Locate every blood parasite and identify its species.
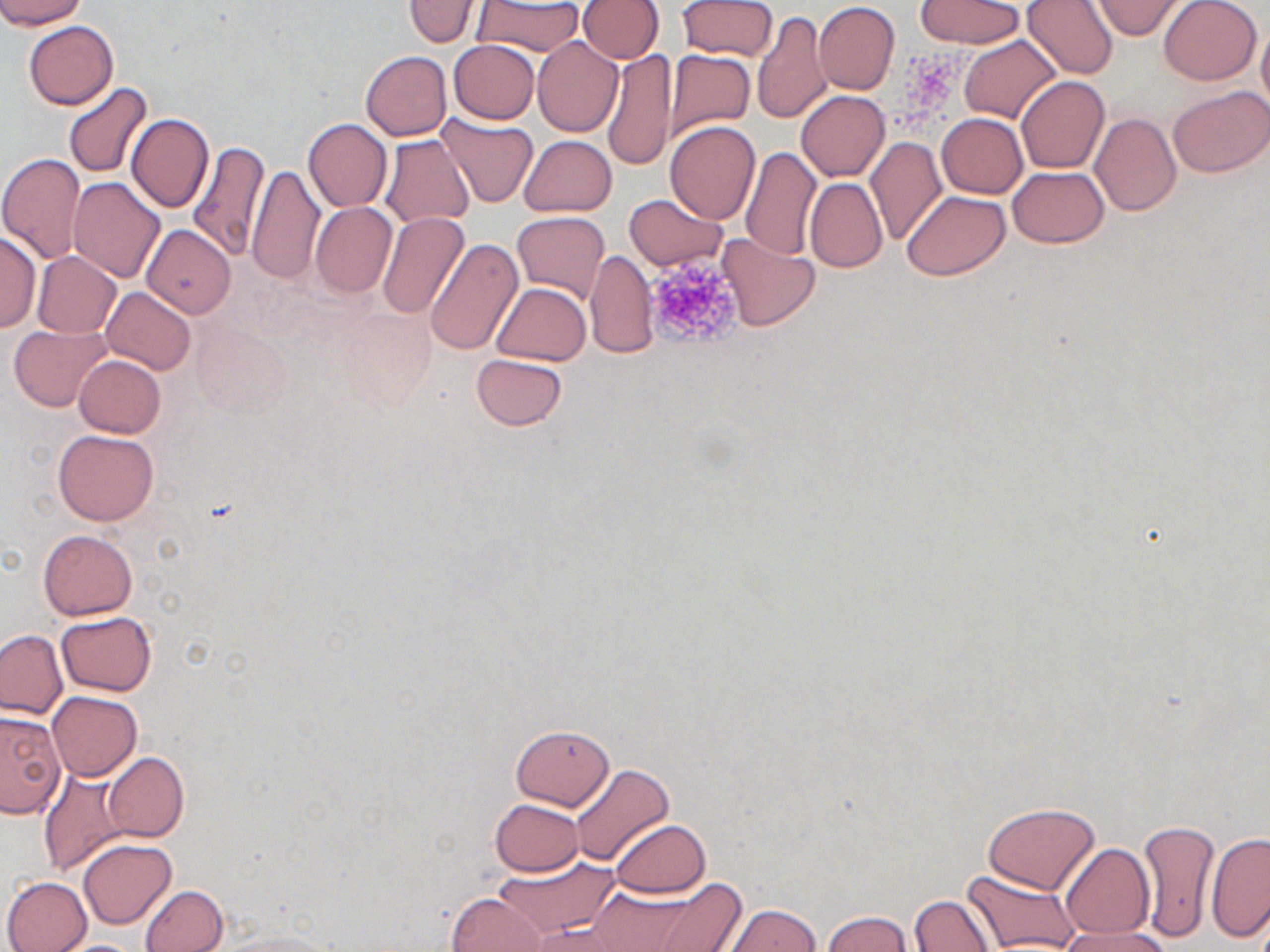
No blood parasites observed.

Summary:
  - Coordinate format: approximate bounding boxes as [x1, y1, x2, y2] in pixels
  - Platelet locations: [644, 255, 745, 350]
  - Uninfected red blood cell locations: [0, 0, 86, 28], [577, 0, 664, 64], [1022, 0, 1119, 79], [1159, 0, 1262, 86], [404, 1, 481, 47], [474, 1, 586, 57], [679, 1, 778, 60], [916, 1, 1026, 48], [1091, 1, 1186, 39], [813, 2, 900, 94], [752, 11, 832, 124], [1257, 19, 1270, 123], [23, 21, 119, 109], [959, 36, 1061, 124], [532, 37, 624, 136], [449, 40, 539, 123], [602, 49, 677, 171], [664, 50, 755, 139], [361, 51, 452, 140], [1016, 77, 1108, 173], [644, 78, 736, 210], [63, 82, 152, 177], [1169, 86, 1270, 178], [797, 90, 889, 181], [436, 112, 538, 208], [936, 113, 1027, 198], [1091, 113, 1180, 215], [126, 114, 214, 213], [303, 118, 391, 211], [664, 120, 760, 223], [379, 134, 474, 229], [519, 135, 617, 217], [864, 136, 946, 247], [186, 141, 271, 261], [741, 147, 821, 261], [0, 154, 87, 265], [247, 163, 324, 287], [1007, 166, 1109, 247], [67, 176, 165, 281], [805, 178, 887, 272], [901, 190, 1010, 279], [624, 194, 727, 271], [311, 203, 397, 298], [512, 211, 610, 303], [376, 213, 469, 319], [140, 225, 236, 318], [0, 230, 40, 333], [716, 232, 820, 331], [424, 238, 525, 355], [585, 250, 656, 358], [31, 251, 122, 338], [491, 282, 591, 365], [101, 285, 195, 375], [193, 320, 292, 416], [9, 324, 111, 412], [471, 353, 567, 431], [74, 354, 165, 438], [53, 429, 158, 525], [40, 529, 138, 619], [55, 612, 156, 695], [0, 629, 67, 719], [47, 690, 142, 780], [0, 709, 65, 818], [510, 722, 615, 811], [104, 752, 188, 842], [570, 762, 675, 866], [39, 767, 130, 877], [489, 799, 584, 875], [982, 802, 1100, 895], [610, 819, 711, 898], [1136, 819, 1220, 941], [1206, 831, 1270, 942], [78, 839, 176, 929], [1060, 844, 1154, 939], [489, 854, 619, 941], [962, 868, 1081, 952], [2, 876, 92, 952], [586, 881, 727, 950], [140, 885, 227, 952], [448, 892, 548, 952], [908, 895, 996, 951], [720, 904, 822, 951], [820, 910, 914, 952], [525, 922, 632, 951], [1059, 924, 1171, 952], [220, 930, 340, 952], [55, 939, 147, 952]
  - Slide-level diagnosis: negative for blood parasites
  - Preparation: thin blood film
  - Modality: optical microscopy
  - Image size: 1270×952 pixels
  - Field of view: single
  - Stain: May-Grünwald-Giemsa
  - Magnification: 1000x